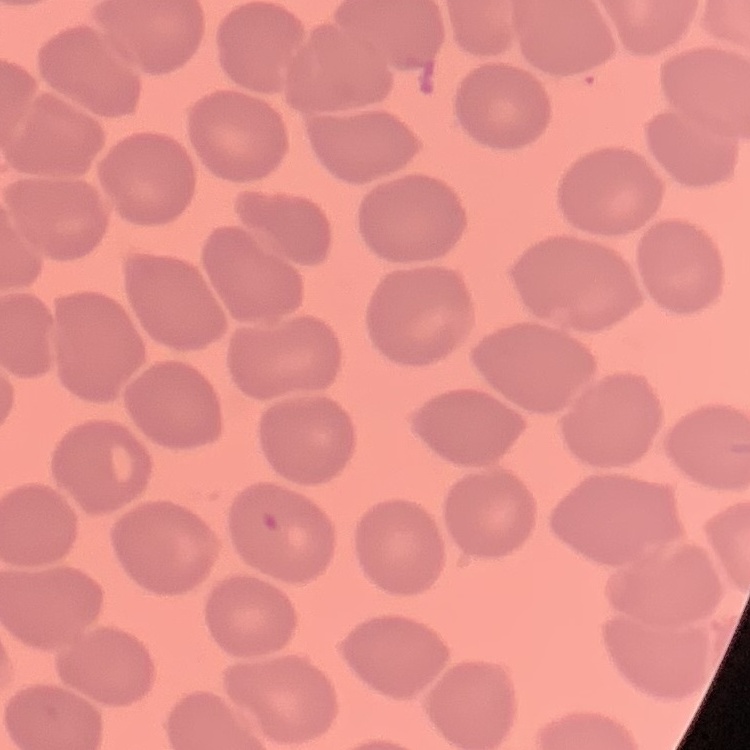

Summary:
  - Erythrocyte morphology: no rouleaux formation
  - Stain: Field's or Giemsa
  - Preparation: thin peripheral smear
  - Image type: one tile cut from a larger photomicrograph